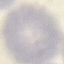
Malaria status: uninfected. Giemsa-stained preparation. Photographed with a smartphone camera at the microscope eyepiece. Automatically extracted cell patch, resized to 64 × 64 pixels. Thin blood film.